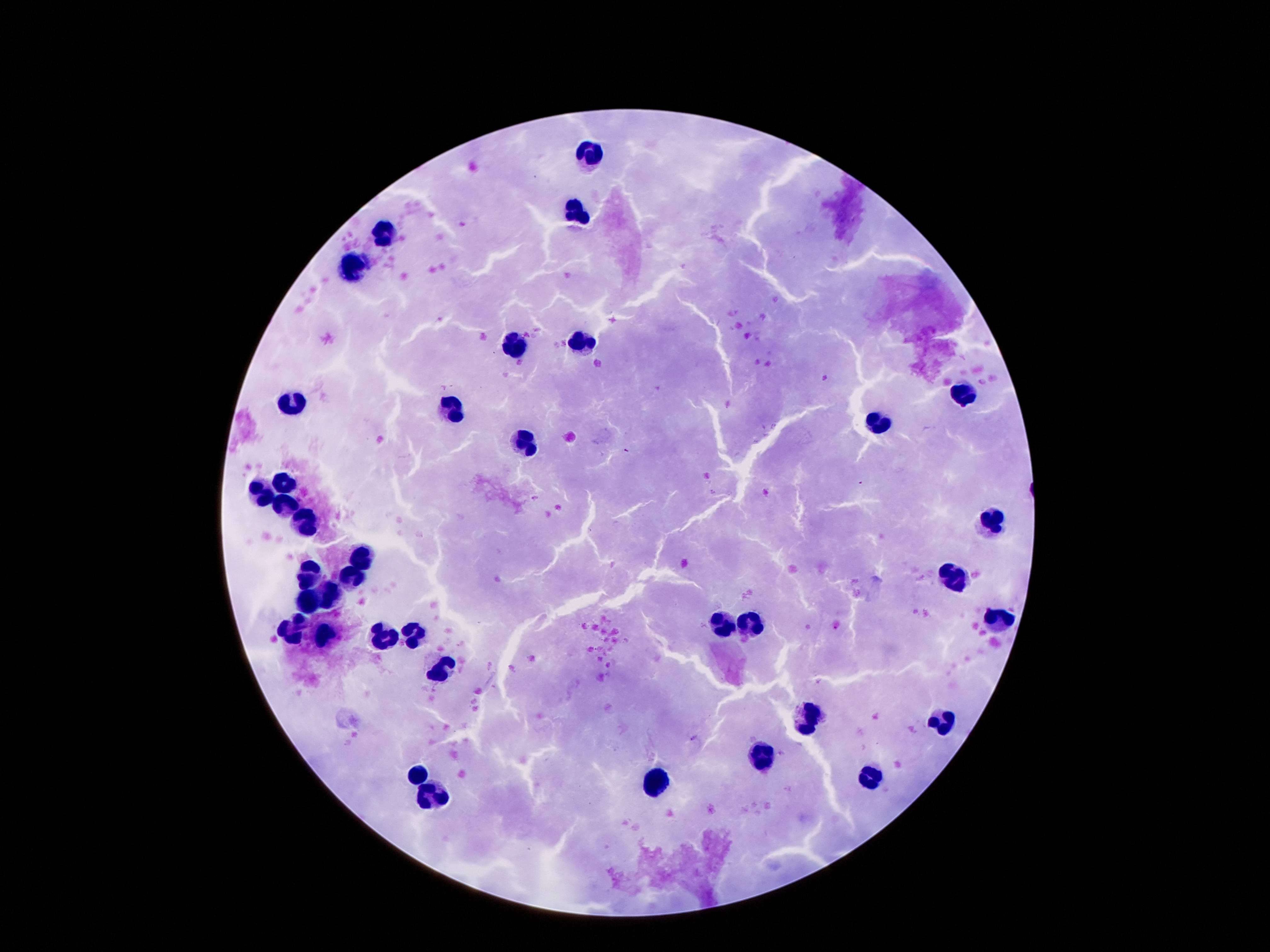
magnification = 100x
patient malaria status = not infected
preparation = thick peripheral-blood smear
field of view = one from this slide
capture = smartphone camera through the microscope eyepiece
image size = 1270×952 pixels
leukocyte locations = approximate centers as (x, y) in pixels: (589, 153), (575, 212), (389, 234), (350, 265), (576, 344), (512, 347), (962, 395), (290, 400), (450, 410), (877, 424), (526, 444), (285, 480), (260, 492), (285, 507), (991, 523), (306, 524), (361, 558), (310, 572), (355, 575), (956, 577), (329, 596), (310, 603), (998, 621), (723, 624), (752, 624), (293, 627), (324, 634), (413, 636), (382, 638), (441, 667), (809, 719), (941, 722), (762, 756), (421, 772), (654, 782), (872, 782), (431, 794)
stain = Giemsa